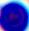

Summary:
  - Modality: photomicrograph
  - Identification: leukocyte
  - Magnification: 400x